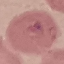

Malaria status: uninfected. Giemsa-stained preparation. Cell patch, automatically extracted from a larger field of view and resized to 64 × 64 pixels. Thin blood film. Photographed with a smartphone camera at the microscope eyepiece.